Assess for malaria.
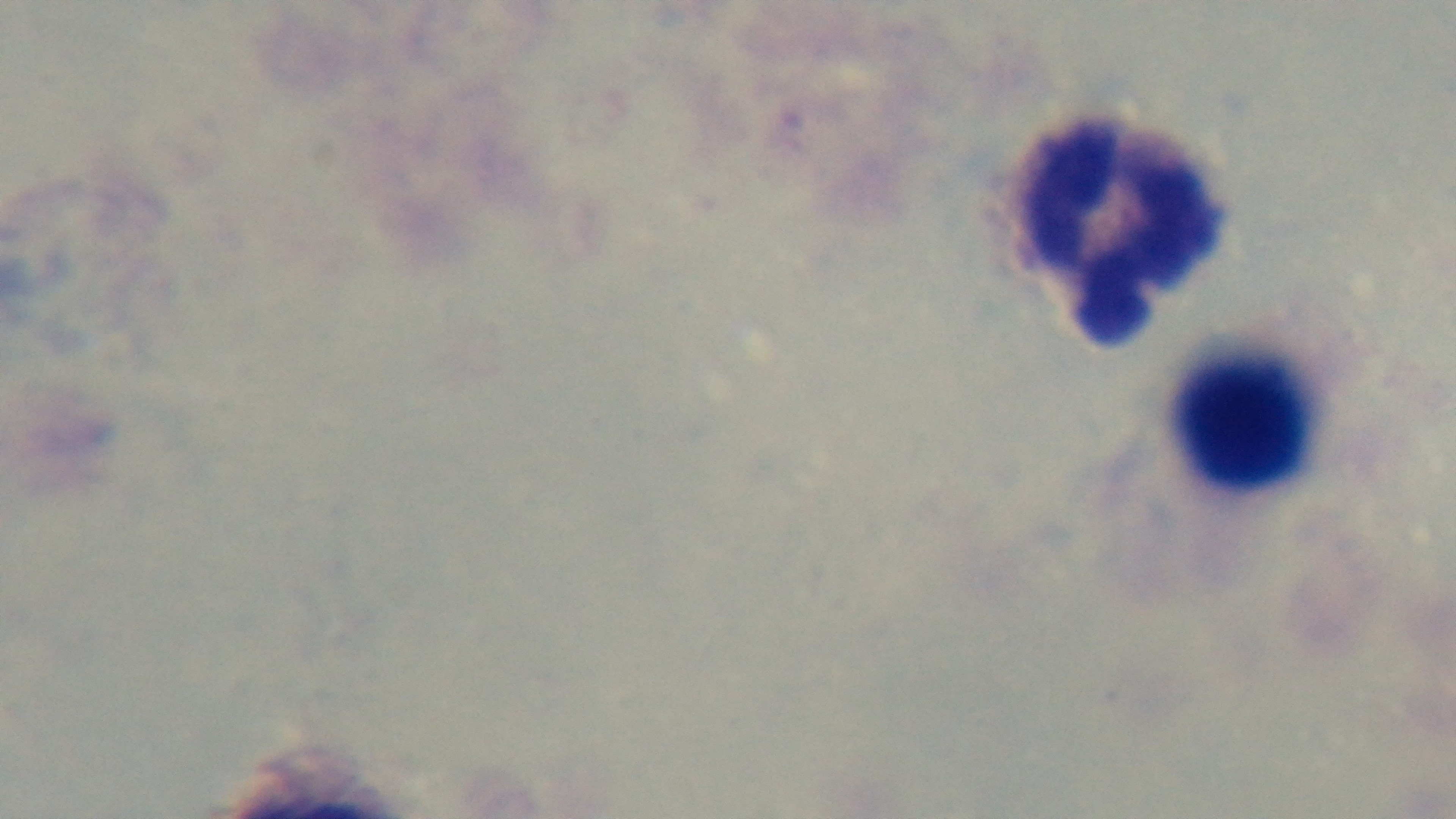
It is uninfected.

capture: mounted 4K digital camera
field_of_view: one from the slide
modality: light microscopy
preparation: thick smear
stain: Giemsa
objective: 100x oil immersion